Name the parasite shown.
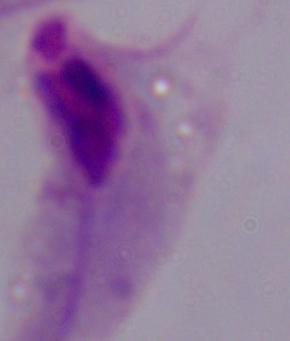
A trichomonad.

magnification = 1000x
modality = micrograph